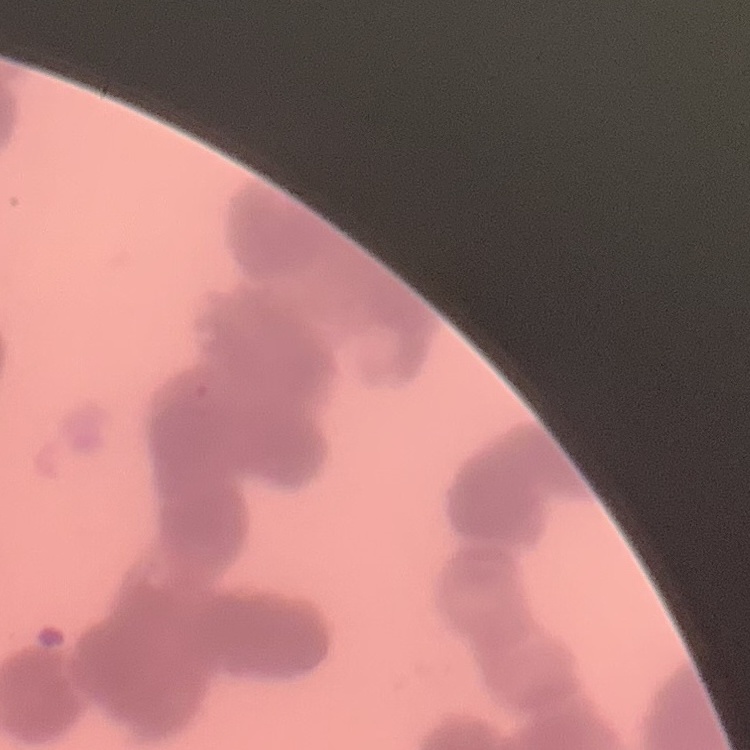
The red blood cells show rouleaux formation. Square crop of a larger photomicrograph. Thin blood film. Field's or Giemsa stain.